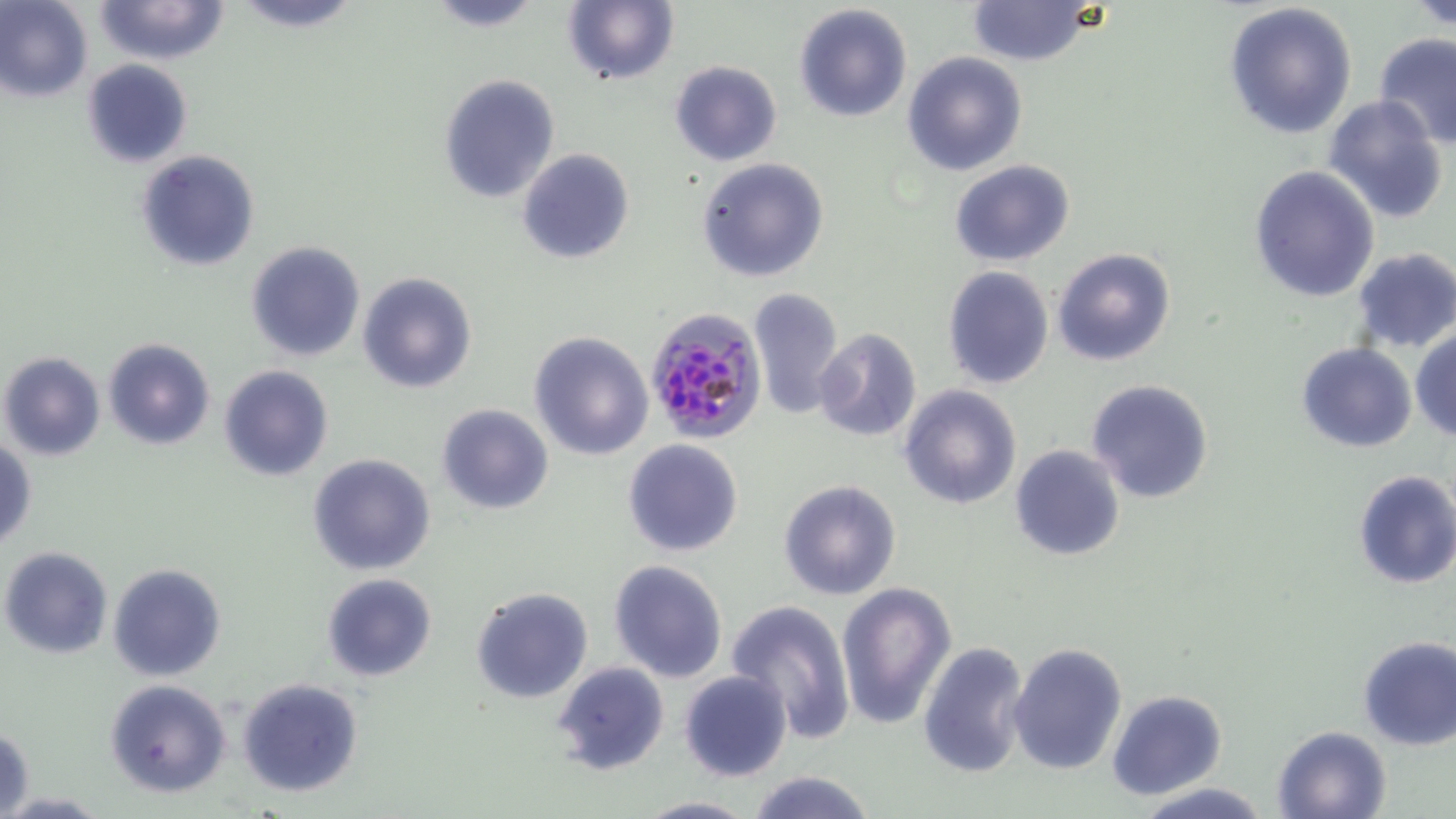
Summary:
  - Coordinate format: approximate bounding boxes as (x1,y1)-(x2,y2) corner pairs in pixels
  - Plasmodium falciparum-infected red blood cell locations: (643,306)-(766,443)
  - Uninfected red blood cell locations: (94,0)-(230,66), (234,0)-(365,32), (421,0)-(548,31), (562,0)-(678,87), (1409,0)-(1455,31), (0,1)-(93,102), (967,1)-(1095,67), (1224,1)-(1358,140), (794,3)-(913,123), (1372,33)-(1456,149), (903,51)-(1029,176), (80,60)-(193,168), (669,60)-(781,166), (439,74)-(561,204), (1322,94)-(1451,224), (517,148)-(635,264), (137,149)-(258,271), (696,158)-(831,283), (951,161)-(1075,267), (1249,165)-(1380,303), (245,240)-(365,361), (1052,246)-(1178,367), (1349,247)-(1456,353), (942,266)-(1053,389), (357,271)-(479,393), (748,286)-(844,418), (813,327)-(923,443), (1410,327)-(1456,442), (529,332)-(654,460), (102,338)-(216,451), (1297,343)-(1417,452), (0,352)-(105,461), (219,364)-(334,481), (1085,378)-(1215,504), (897,383)-(1023,510), (436,403)-(554,515), (622,438)-(744,556), (0,440)-(37,549), (1009,444)-(1126,563), (307,453)-(437,576), (1352,469)-(1456,590), (779,479)-(901,600), (1,546)-(115,659), (608,560)-(727,683), (107,563)-(228,682), (321,573)-(437,681), (838,582)-(956,730), (470,587)-(594,703), (725,599)-(856,739), (1356,636)-(1456,751), (917,641)-(1031,778), (1008,642)-(1127,775), (553,662)-(670,778), (678,670)-(793,781), (236,677)-(365,800), (104,678)-(233,798), (1106,688)-(1228,801), (1,725)-(35,819), (1271,726)-(1391,818), (742,771)-(878,819), (1130,780)-(1275,818), (635,794)-(756,818)
  - Slide-level diagnosis: Plasmodium falciparum
  - Image size: 1456×819 pixels
  - Preparation: thin blood smear
  - Stain: May-Grünwald-Giemsa
  - Modality: light microscopy
  - Field of view: single
  - Magnification: 1000x